Name the parasite shown.
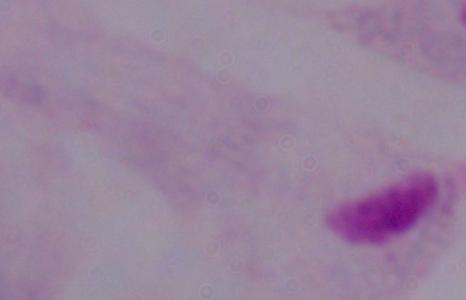

A trichomonad.

Summary:
  - Magnification: 1000x
  - Modality: photomicrograph